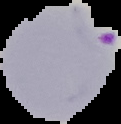

From a thin blood smear. Image is 121×124 pixels. Result: Plasmodium parasites identified. Segmented cell region on a black background.